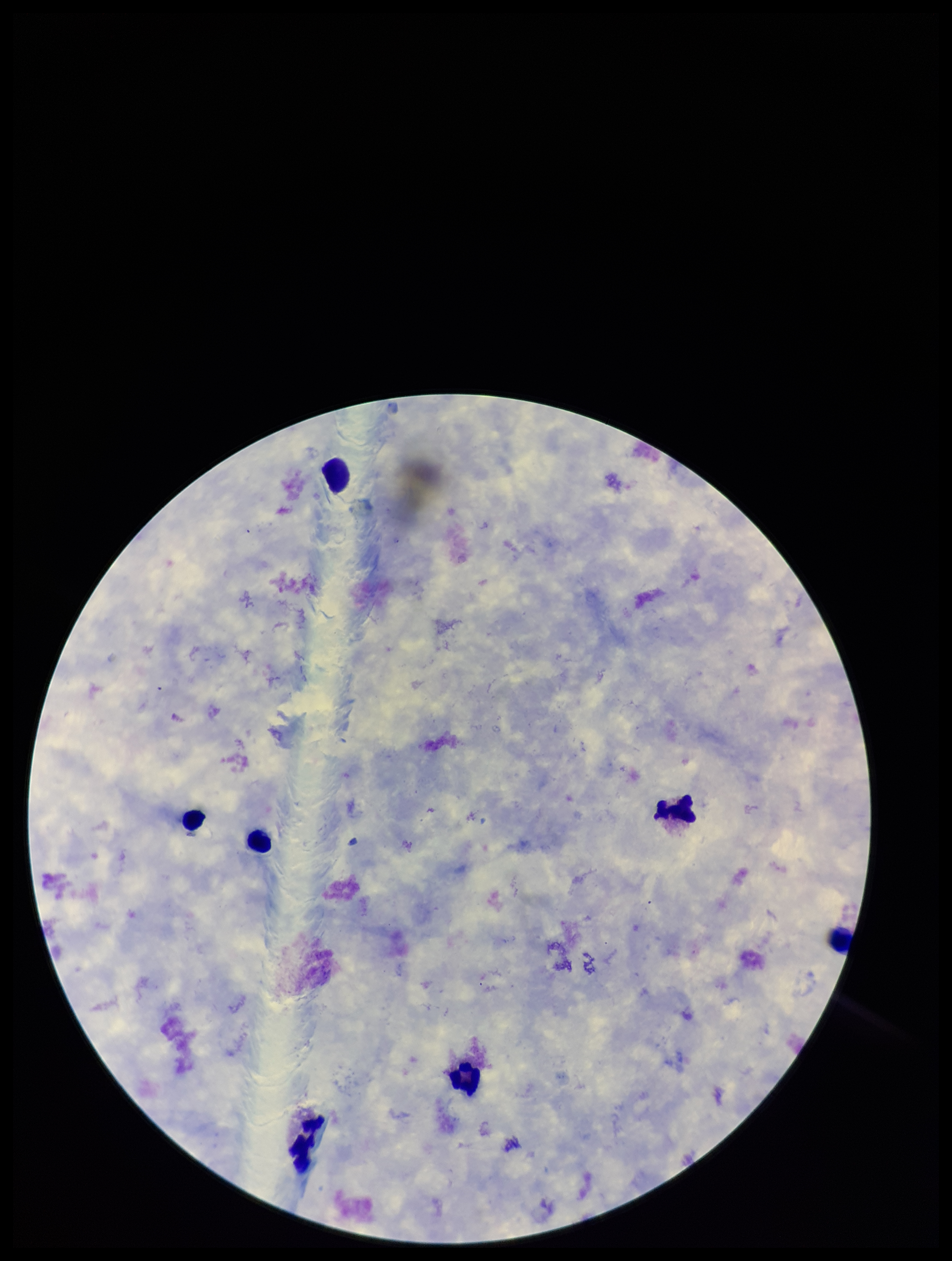

stain = Giemsa
parasite count = 0
patient malaria status = negative
capture = smartphone photograph through the microscope eyepiece
image size = 952×1261 pixels
field of view = single
leukocyte count = 7
Plasmodium parasites = none seen
preparation = thick